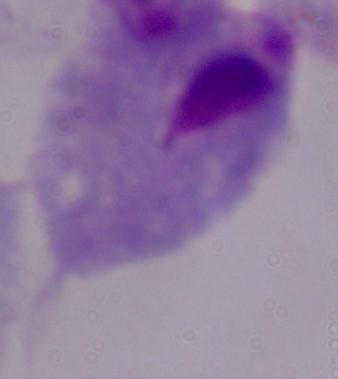

Captured at 1000x magnification. A trichomonad is shown. Photomicrograph.